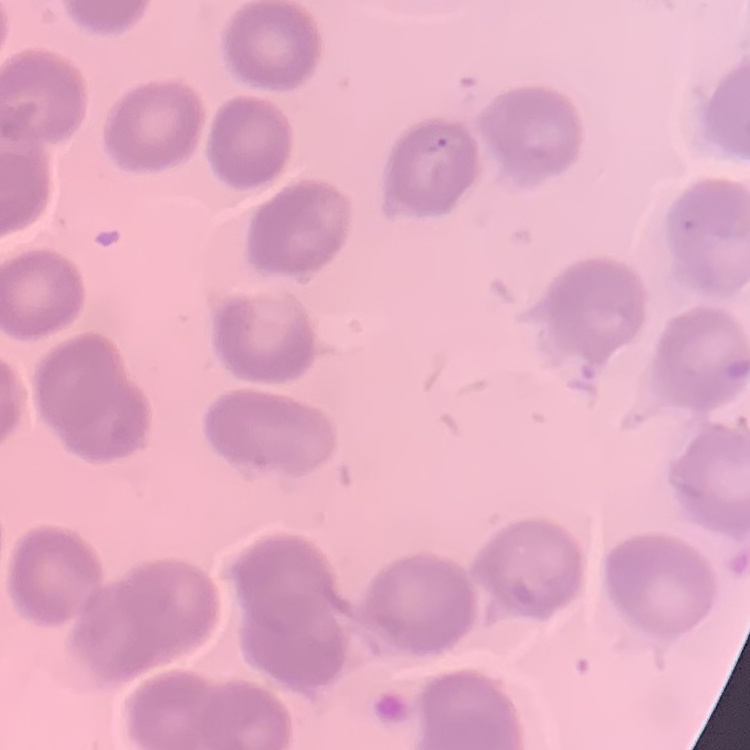
The erythrocytes exhibit no rouleaux formation. Thin blood film. One tile cut from a larger photomicrograph. Field's or Giemsa stain.